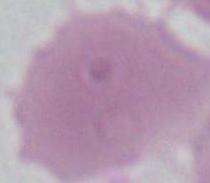

Summary:
  - Identification: red blood cell
  - Modality: photomicrograph
  - Magnification: 1000x